Name the blood parasite species.
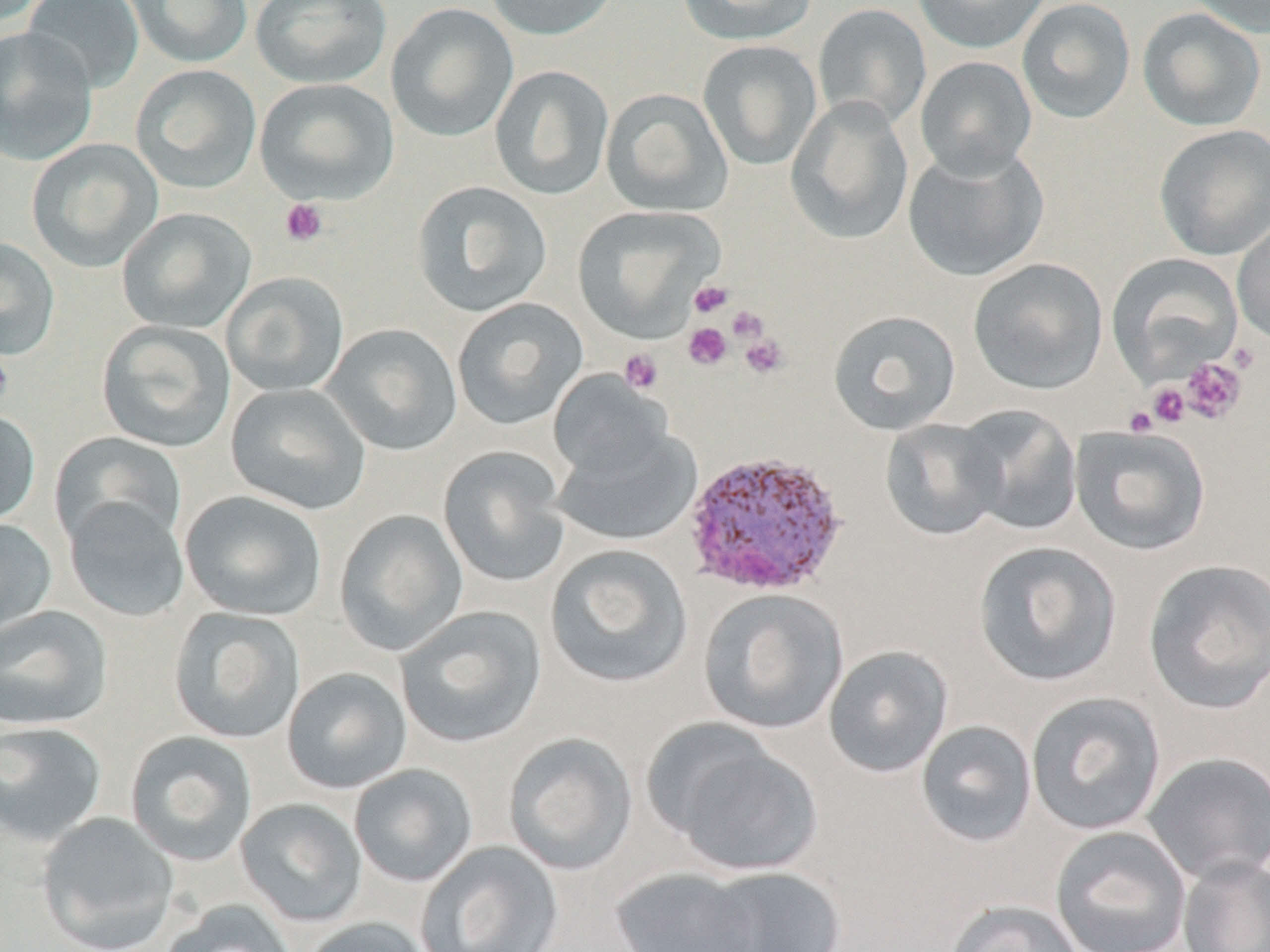
Plasmodium vivax.

Summary:
  - Coordinate format: approximate bounding boxes as (x1, y1, x2, y2) in pixels
  - Plasmodium vivax-infected red blood cell locations: (682, 448, 848, 598)
  - Platelet locations: (279, 197, 329, 247), (689, 280, 733, 318), (728, 306, 768, 344), (683, 323, 732, 370), (739, 332, 789, 379), (0, 339, 14, 415), (619, 348, 664, 394), (1180, 357, 1246, 423), (1148, 384, 1190, 427), (1124, 406, 1158, 435)
  - Uninfected red blood cell locations: (22, 0, 144, 92), (121, 0, 253, 68), (250, 0, 392, 88), (484, 0, 621, 41), (676, 0, 817, 46), (912, 0, 1051, 54), (1016, 0, 1136, 123), (1185, 0, 1270, 38), (385, 3, 518, 143), (812, 4, 931, 131), (1137, 8, 1266, 131), (0, 26, 98, 166), (697, 39, 822, 171), (915, 55, 1037, 180), (130, 64, 261, 194), (489, 65, 614, 201), (255, 78, 399, 205), (600, 88, 733, 217), (785, 96, 914, 246), (1153, 124, 1270, 261), (27, 138, 163, 272), (903, 144, 1048, 282), (411, 180, 552, 317), (571, 204, 724, 342), (116, 207, 256, 334), (1232, 215, 1270, 347), (0, 237, 60, 360), (1107, 253, 1242, 383), (968, 258, 1108, 394), (221, 271, 349, 397), (452, 297, 588, 430), (827, 309, 961, 435), (96, 319, 236, 452), (322, 323, 462, 456), (548, 369, 672, 482), (225, 383, 372, 516), (955, 404, 1083, 536), (0, 409, 40, 529), (879, 417, 1006, 540), (1070, 425, 1211, 555), (551, 428, 701, 547), (49, 431, 187, 551), (437, 446, 571, 588), (180, 490, 327, 621), (63, 498, 190, 623), (334, 510, 468, 656), (0, 517, 57, 637), (973, 541, 1122, 687), (545, 544, 693, 689), (1142, 559, 1270, 714), (698, 587, 849, 735), (0, 605, 113, 731), (395, 606, 546, 749), (168, 607, 306, 744), (823, 644, 953, 778), (281, 666, 413, 795), (1026, 692, 1166, 835), (915, 719, 1038, 848), (0, 721, 108, 847), (125, 731, 258, 867), (503, 732, 638, 876), (662, 735, 823, 877), (1141, 751, 1270, 884), (349, 764, 478, 887), (235, 798, 366, 928), (36, 811, 179, 952), (1050, 825, 1192, 952), (415, 841, 564, 952), (1177, 855, 1270, 952), (699, 866, 846, 952), (611, 867, 764, 952), (945, 899, 1086, 952), (158, 900, 296, 952), (299, 917, 433, 952)
  - Preparation: thin blood smear
  - Modality: optical microscopy
  - Field of view: one of a larger specimen
  - Magnification: 1000x
  - Stain: May-Grünwald-Giemsa
  - Image size: 1270×952 pixels